Report the malaria status of this cell.
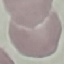
Uninfected.

{
  "capture": "smartphone camera at the microscope eyepiece",
  "preparation": "thin smear",
  "image_type": "cell patch, automatically extracted from a larger field of view and resized to 64 × 64 pixels",
  "stain": "Giemsa"
}